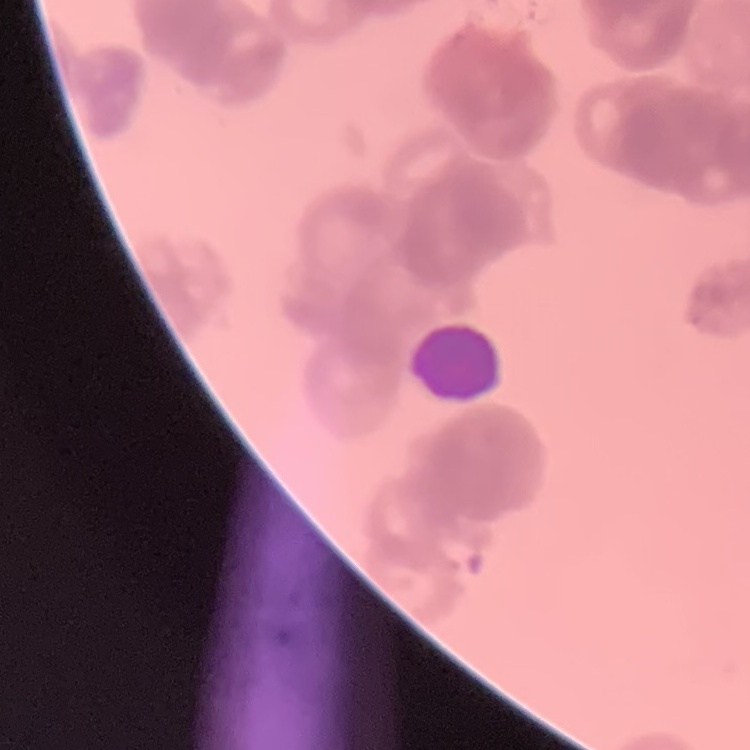 The red blood cells show rouleaux formation. Thin peripheral smear. Square crop of a larger photomicrograph. Field's or Giemsa stain.